Report the malaria status of this cell.
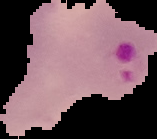

It is parasitized.

Image is 157×139 pixels. From a thin blood film. Segmented cell region on a black background.